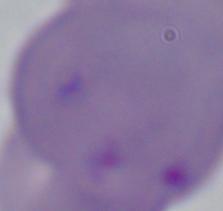

Captured at 1000x magnification. Photomicrograph. A Babesia parasite is shown.